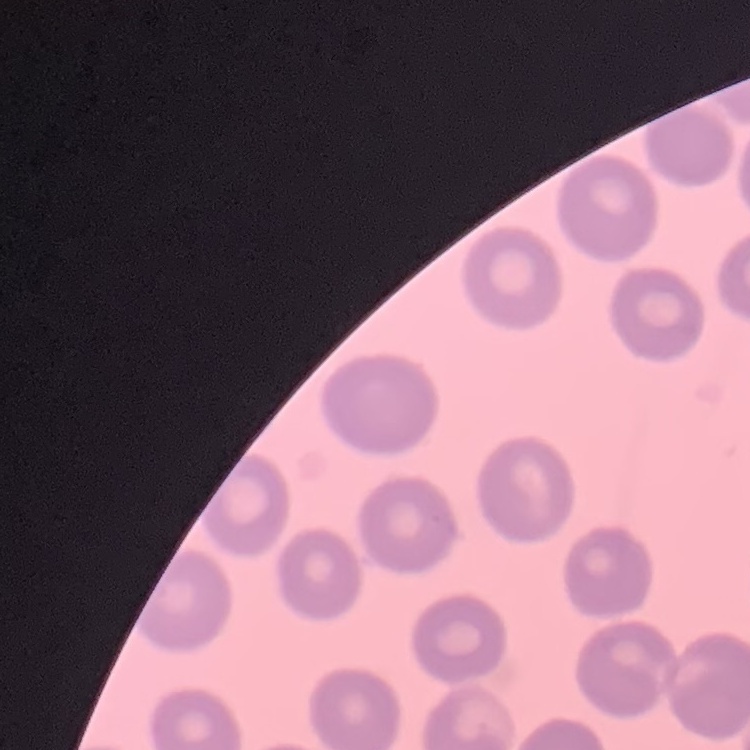

The erythrocytes exhibit no rouleaux formation. Field's or Giemsa stain. Square crop of a larger photomicrograph. Thin blood film.